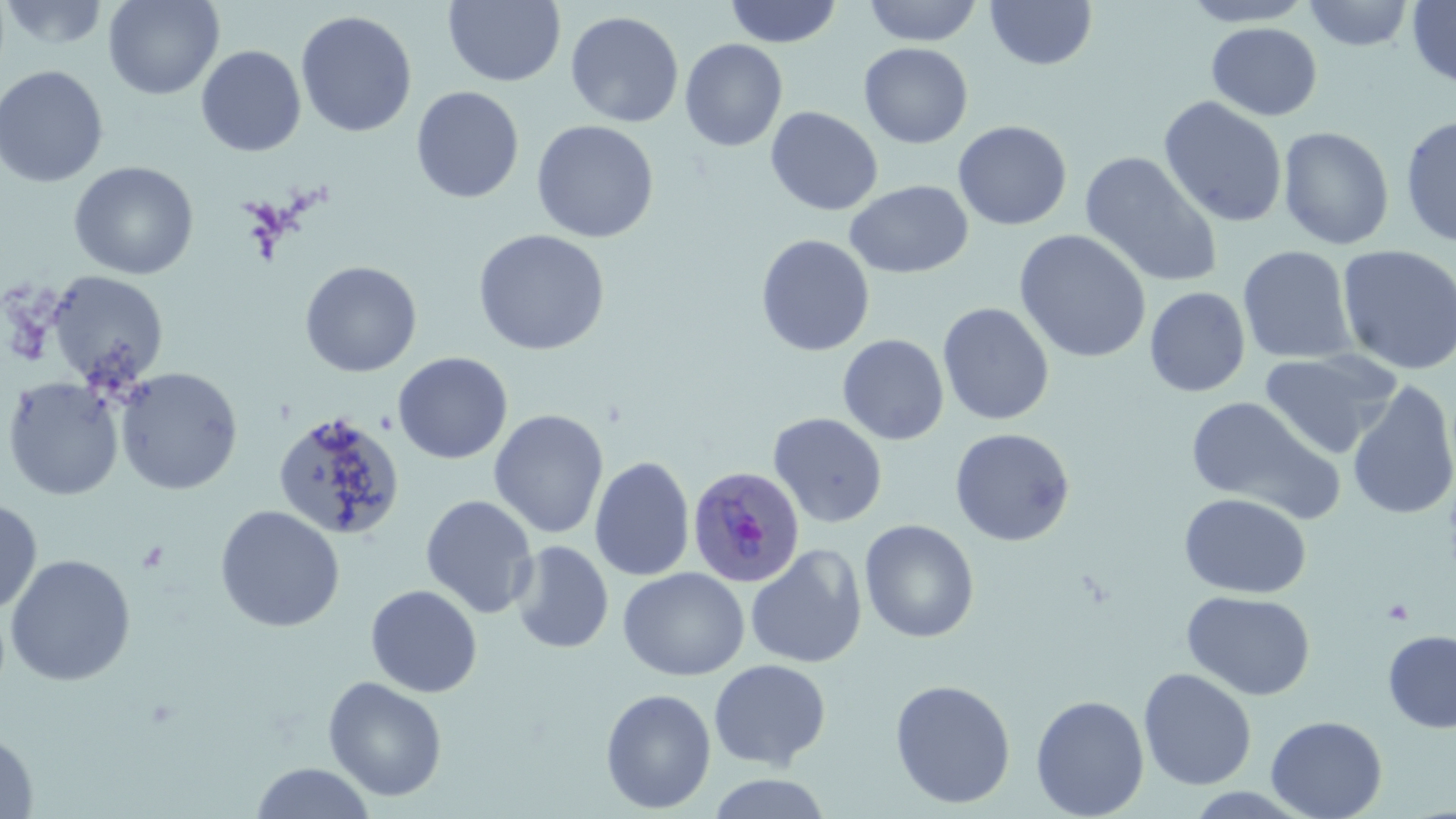

{
  "slide_level_diagnosis": "Plasmodium ovale",
  "uninfected_red_blood_cell_locations": "approximate bounding boxes as [x1, y1, x2, y2] in pixels: [103, 0, 224, 99], [724, 0, 842, 47], [862, 0, 983, 46], [985, 0, 1097, 71], [1182, 0, 1315, 28], [1303, 0, 1415, 52], [0, 1, 111, 51], [443, 1, 566, 87], [1406, 1, 1456, 89], [295, 10, 417, 138], [564, 10, 684, 128], [1206, 23, 1323, 121], [679, 39, 788, 152], [858, 43, 973, 148], [196, 45, 307, 157], [0, 65, 108, 188], [410, 86, 524, 204], [1158, 96, 1288, 228], [765, 106, 883, 216], [1399, 114, 1456, 247], [531, 120, 659, 243], [953, 120, 1072, 231], [1278, 126, 1395, 251], [1080, 151, 1223, 288], [68, 161, 199, 280], [845, 180, 972, 278], [473, 229, 610, 356], [1014, 229, 1152, 363], [755, 234, 875, 356], [1237, 245, 1357, 364], [1336, 245, 1456, 376], [300, 260, 422, 377], [46, 271, 168, 388], [1144, 287, 1251, 397], [937, 302, 1054, 425], [837, 334, 949, 445], [1258, 349, 1403, 460], [393, 352, 513, 464], [115, 367, 243, 495], [2, 376, 124, 501], [1346, 380, 1456, 521], [1185, 396, 1343, 522], [489, 409, 609, 539], [272, 411, 405, 541], [769, 412, 888, 528], [950, 427, 1075, 546], [590, 456, 695, 581], [1179, 492, 1311, 598], [420, 495, 539, 619], [0, 498, 42, 615], [215, 505, 345, 633], [463, 518, 594, 637], [859, 519, 980, 643], [509, 540, 615, 654], [746, 544, 867, 669], [5, 554, 136, 686], [618, 567, 749, 681], [365, 584, 482, 698], [1182, 590, 1316, 701], [1383, 630, 1456, 733], [708, 658, 831, 770], [1138, 667, 1257, 790], [323, 676, 447, 801], [889, 678, 1016, 809], [600, 688, 717, 814], [1030, 694, 1150, 819], [1266, 715, 1387, 819], [0, 732, 38, 817], [250, 762, 376, 819], [704, 772, 833, 818]",
  "preparation": "thin blood smear",
  "magnification": "1000x",
  "field_of_view": "one of a larger specimen",
  "image_size": "1456×819 pixels",
  "stain": "May-Grünwald-Giemsa",
  "modality": "optical microscopy",
  "plasmodium_ovale_infected_red_blood_cell_locations": "approximate bounding boxes as [x1, y1, x2, y2] in pixels: [688, 465, 805, 587]",
  "platelet_locations": "approximate bounding boxes as [x1, y1, x2, y2] in pixels: [135, 540, 169, 574]"
}